Evaluate for Plasmodium parasites.
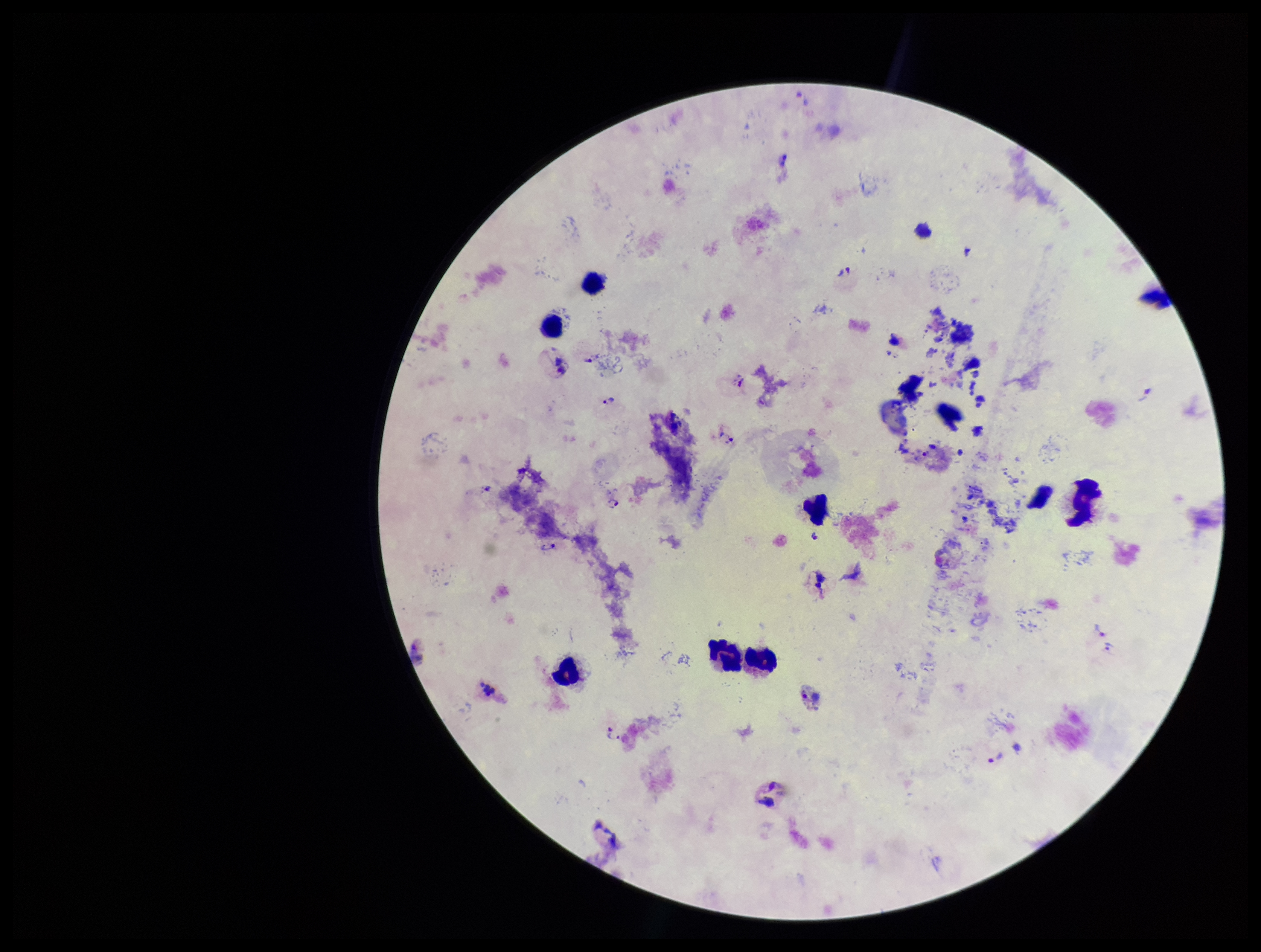

Identified.

Summary:
  - Image size: 1261×952 pixels
  - Species reported for this patient: Plasmodium vivax
  - Capture: smartphone photograph through the microscope eyepiece
  - Field of view: one from this slide
  - Patient malaria status: infected
  - Stain: Giemsa
  - Parasite count: 10
  - Leukocyte count: 10
  - Preparation: thick smear